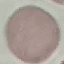

Summary:
  - Result: negative for malaria parasites
  - Image type: automatically extracted cell patch, resized to 64 × 64 pixels
  - Preparation: thin smear
  - Capture: smartphone through the microscope eyepiece
  - Stain: Giemsa